Report the malaria status of this cell.
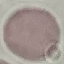

It is uninfected.

{
  "preparation": "thin smear",
  "stain": "Giemsa",
  "image_type": "cell patch, automatically extracted from a larger field of view and resized to 64 × 64 pixels",
  "capture": "smartphone through the microscope eyepiece"
}